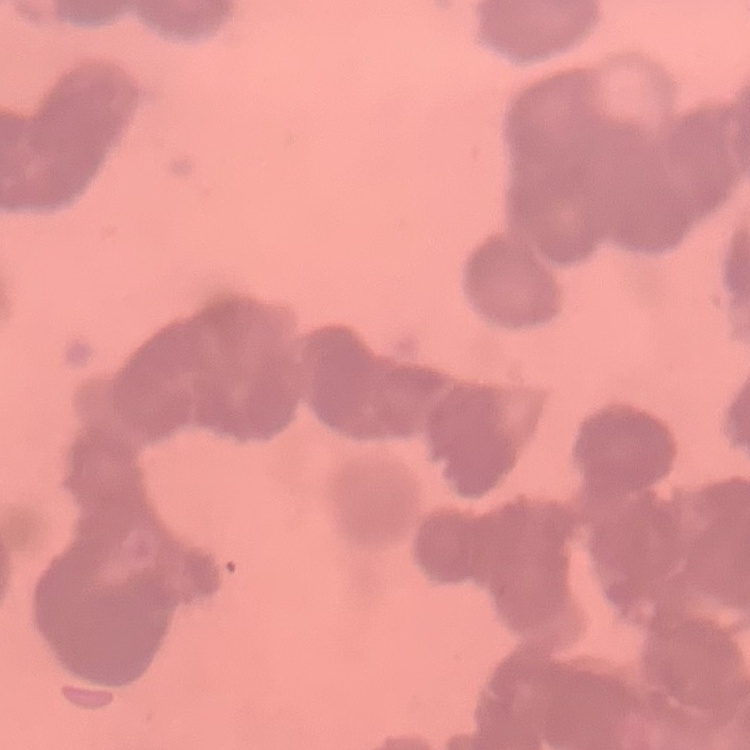
Summary:
  - Erythrocyte morphology: rouleaux formation
  - Image type: square crop of a larger photomicrograph
  - Stain: Field's or Giemsa
  - Preparation: thin blood film